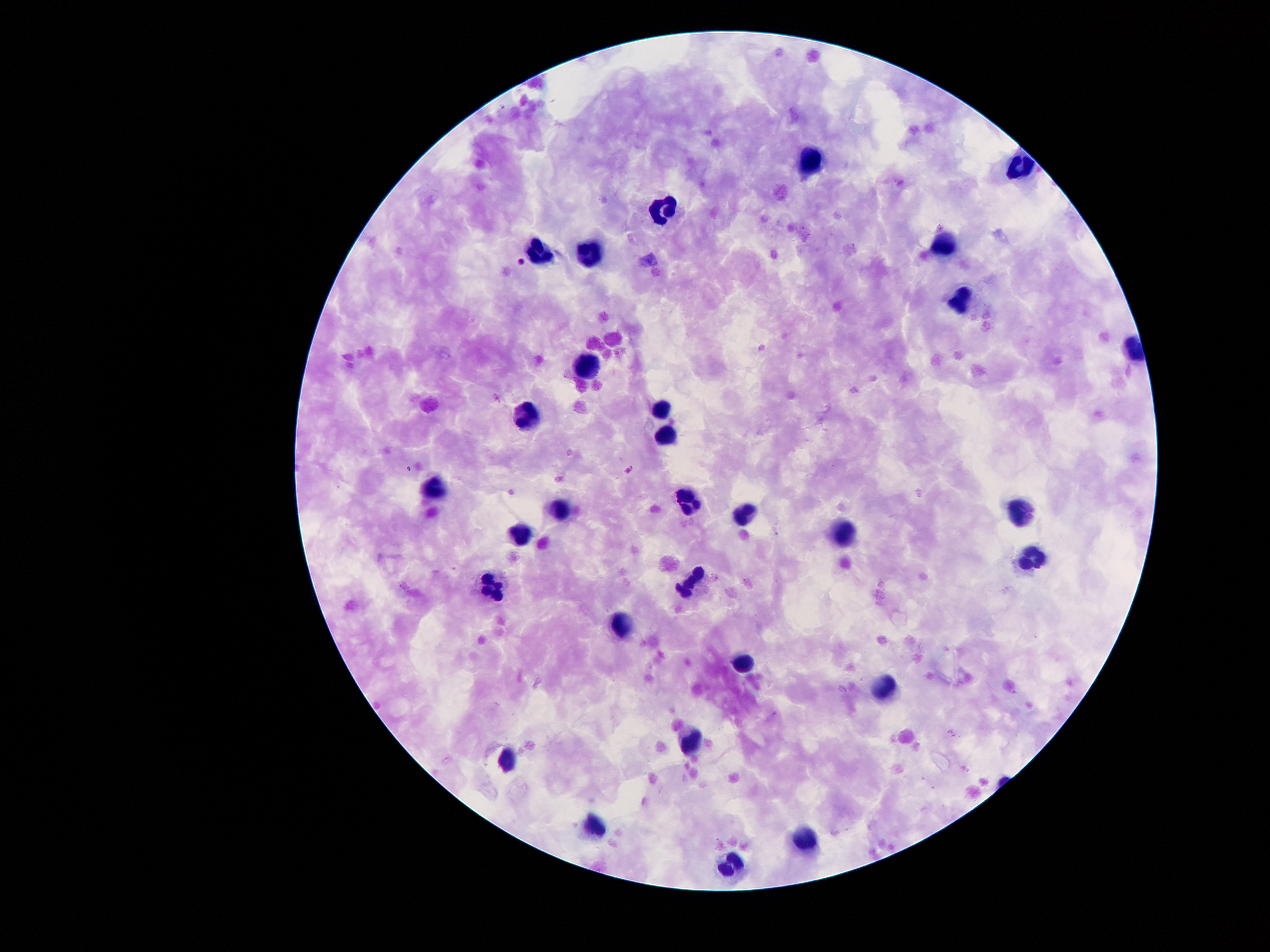
Approximate centers as {x, y} in pixels. Malaria parasite locations: {628, 470}, {952, 732}. Leukocyte locations: {807, 158}, {1026, 166}, {665, 206}, {944, 243}, {539, 250}, {588, 255}, {960, 301}, {586, 366}, {527, 411}, {663, 413}, {663, 438}, {435, 485}, {692, 509}, {559, 510}, {1021, 511}, {743, 513}, {520, 531}, {844, 531}, {1030, 556}, {691, 581}, {491, 585}, {626, 619}, {745, 661}, {884, 687}, {688, 740}, {509, 760}, {594, 823}, {809, 836}, {730, 862}. Smartphone photograph taken through the microscope eyepiece. Giemsa-stained preparation. One field from this slide. Thick peripheral-blood smear. Image is 1270×952 pixels. 100x magnification. Patient malaria status: infected with Plasmodium falciparum.